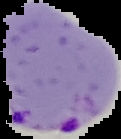
{
  "result": "Plasmodium parasites identified",
  "preparation": "thin blood smear",
  "image_size": "121×139 pixels",
  "image_type": "cell region segmented out of the field of view; surrounding area masked to black"
}